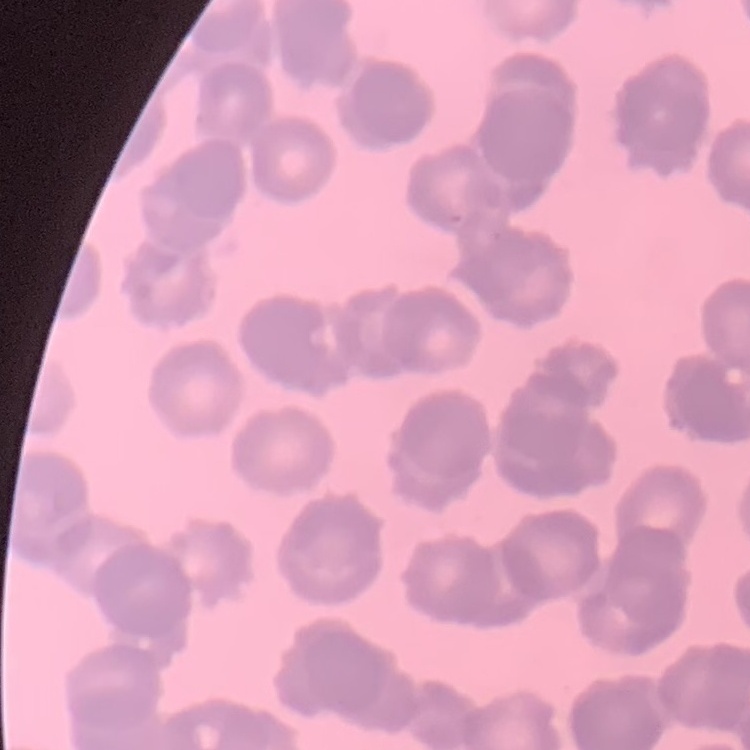 The erythrocytes exhibit rouleaux formation. Thin peripheral smear. Field's or Giemsa stain. One tile cut from a larger photomicrograph.